Outline each blood parasite and name the species.
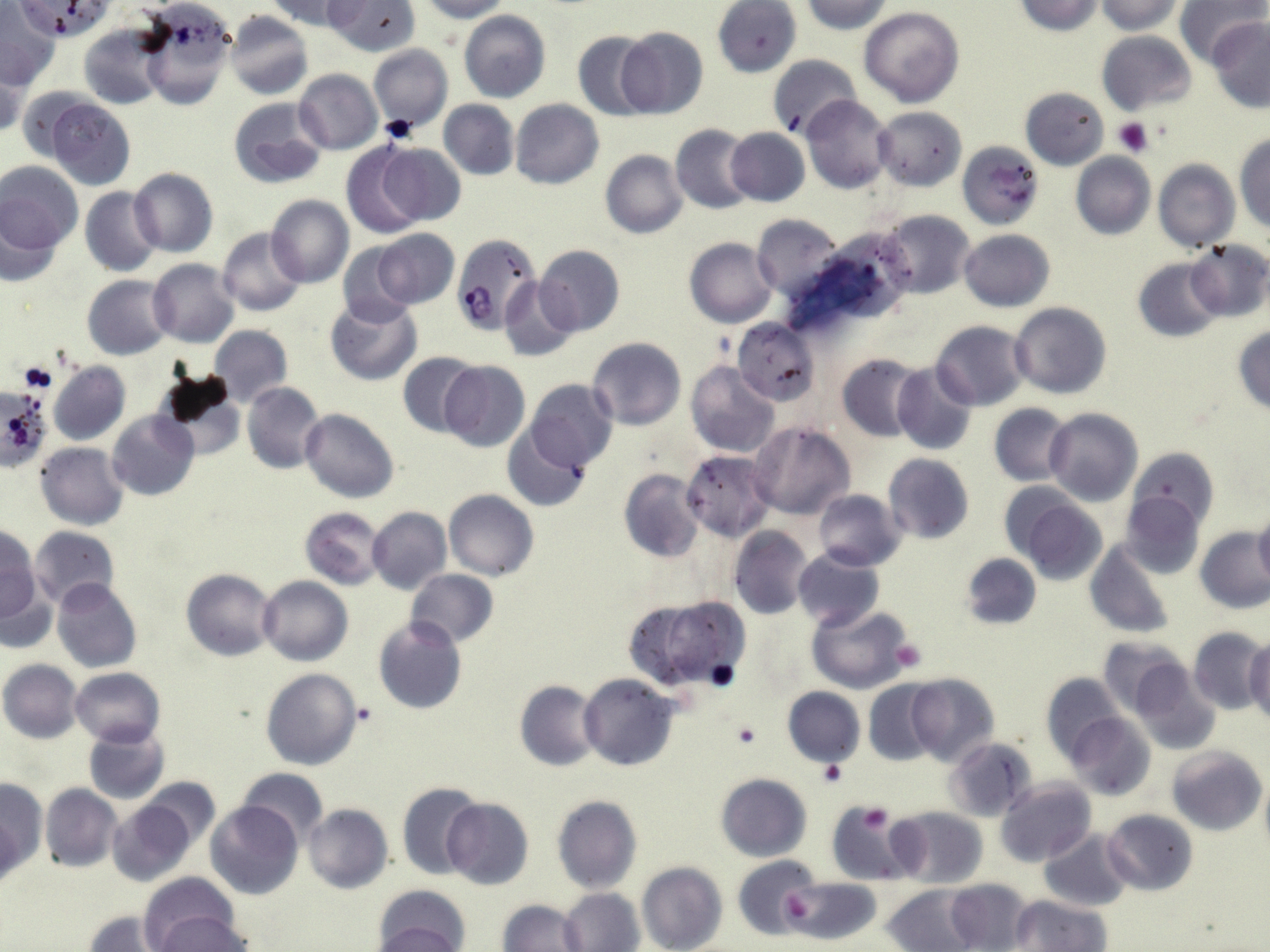

Approximate bounding boxes as named x1/y1/x2/y2 corners in pixels.
Plasmodium falciparum-infected red blood cells: (x1=451, y1=234, x2=542, y2=332).
No Plasmodium ovale, Plasmodium malariae, Plasmodium vivax, Babesia divergens, or Trypanosoma brucei observed.

slide_level_diagnosis: Plasmodium falciparum
uninfected_red_blood_cell_locations: 'approximate bounding boxes as named x1/y1/x2/y2 corners in pixels: (x1=15, y1=0, x2=111, y2=40), (x1=266, y1=0, x2=355, y2=30), (x1=324, y1=0, x2=420, y2=55), (x1=418, y1=0, x2=513, y2=21), (x1=712, y1=0, x2=800, y2=77), (x1=799, y1=0, x2=896, y2=34), (x1=1013, y1=0, x2=1103, y2=35), (x1=1097, y1=0, x2=1185, y2=34), (x1=1176, y1=0, x2=1264, y2=65), (x1=135, y1=4, x2=235, y2=111), (x1=0, y1=5, x2=58, y2=87), (x1=859, y1=6, x2=964, y2=106), (x1=224, y1=9, x2=313, y2=99), (x1=459, y1=10, x2=551, y2=103), (x1=451, y1=11, x2=536, y2=183), (x1=1208, y1=18, x2=1270, y2=113), (x1=80, y1=23, x2=168, y2=109), (x1=615, y1=26, x2=709, y2=119), (x1=573, y1=30, x2=657, y2=120), (x1=1096, y1=31, x2=1198, y2=117), (x1=369, y1=44, x2=452, y2=133), (x1=0, y1=49, x2=28, y2=138), (x1=767, y1=54, x2=862, y2=139), (x1=293, y1=69, x2=382, y2=155), (x1=14, y1=85, x2=95, y2=163), (x1=1019, y1=87, x2=1109, y2=168), (x1=801, y1=95, x2=894, y2=195), (x1=46, y1=97, x2=137, y2=190), (x1=227, y1=97, x2=327, y2=190), (x1=439, y1=99, x2=519, y2=179), (x1=510, y1=99, x2=603, y2=189), (x1=874, y1=106, x2=966, y2=190), (x1=671, y1=124, x2=758, y2=214), (x1=725, y1=128, x2=810, y2=206), (x1=1234, y1=131, x2=1270, y2=233), (x1=958, y1=137, x2=1045, y2=228), (x1=376, y1=142, x2=466, y2=226), (x1=341, y1=143, x2=430, y2=238), (x1=601, y1=150, x2=688, y2=239), (x1=1071, y1=152, x2=1154, y2=239), (x1=1153, y1=158, x2=1239, y2=252), (x1=1, y1=162, x2=83, y2=256), (x1=129, y1=167, x2=218, y2=257), (x1=80, y1=187, x2=162, y2=277), (x1=266, y1=196, x2=353, y2=288), (x1=0, y1=202, x2=68, y2=287), (x1=878, y1=210, x2=977, y2=300), (x1=753, y1=213, x2=844, y2=301), (x1=217, y1=228, x2=306, y2=317), (x1=371, y1=228, x2=460, y2=310), (x1=959, y1=229, x2=1055, y2=312), (x1=685, y1=237, x2=778, y2=327), (x1=1184, y1=241, x2=1270, y2=322), (x1=336, y1=242, x2=418, y2=326), (x1=535, y1=244, x2=626, y2=335), (x1=1132, y1=257, x2=1223, y2=342), (x1=148, y1=260, x2=239, y2=348), (x1=83, y1=274, x2=175, y2=358), (x1=500, y1=276, x2=579, y2=361), (x1=325, y1=294, x2=423, y2=386), (x1=1008, y1=301, x2=1112, y2=399), (x1=732, y1=318, x2=819, y2=405), (x1=930, y1=321, x2=1030, y2=411), (x1=1232, y1=325, x2=1270, y2=416), (x1=209, y1=326, x2=292, y2=407), (x1=588, y1=337, x2=686, y2=431), (x1=398, y1=352, x2=482, y2=438), (x1=837, y1=353, x2=927, y2=441), (x1=48, y1=361, x2=130, y2=445), (x1=439, y1=361, x2=530, y2=453), (x1=685, y1=361, x2=780, y2=458), (x1=892, y1=363, x2=979, y2=455), (x1=153, y1=371, x2=246, y2=460), (x1=525, y1=378, x2=619, y2=471), (x1=242, y1=382, x2=325, y2=473), (x1=989, y1=403, x2=1073, y2=484), (x1=1044, y1=408, x2=1143, y2=505), (x1=301, y1=409, x2=399, y2=503), (x1=107, y1=411, x2=199, y2=501), (x1=748, y1=421, x2=856, y2=521), (x1=503, y1=424, x2=592, y2=513), (x1=36, y1=442, x2=129, y2=530), (x1=1127, y1=447, x2=1219, y2=534), (x1=680, y1=450, x2=773, y2=540), (x1=884, y1=453, x2=974, y2=544), (x1=618, y1=469, x2=705, y2=563), (x1=443, y1=489, x2=540, y2=580), (x1=814, y1=489, x2=904, y2=571), (x1=1120, y1=490, x2=1206, y2=579), (x1=1014, y1=494, x2=1108, y2=586), (x1=299, y1=507, x2=385, y2=588), (x1=366, y1=507, x2=452, y2=595), (x1=1253, y1=510, x2=1270, y2=587), (x1=0, y1=526, x2=42, y2=628), (x1=29, y1=526, x2=119, y2=611), (x1=730, y1=527, x2=815, y2=619), (x1=1195, y1=528, x2=1270, y2=614), (x1=1085, y1=539, x2=1177, y2=638), (x1=793, y1=548, x2=884, y2=628), (x1=959, y1=553, x2=1041, y2=631), (x1=181, y1=569, x2=278, y2=661), (x1=405, y1=569, x2=499, y2=647), (x1=0, y1=576, x2=56, y2=655), (x1=258, y1=576, x2=353, y2=666), (x1=53, y1=577, x2=142, y2=673), (x1=629, y1=593, x2=749, y2=688), (x1=806, y1=602, x2=916, y2=692), (x1=372, y1=615, x2=467, y2=714), (x1=1187, y1=627, x2=1266, y2=716), (x1=1098, y1=636, x2=1190, y2=717), (x1=1246, y1=638, x2=1270, y2=726), (x1=1, y1=660, x2=83, y2=743), (x1=1129, y1=663, x2=1222, y2=756), (x1=70, y1=667, x2=164, y2=747), (x1=262, y1=668, x2=363, y2=770), (x1=904, y1=672, x2=1000, y2=766), (x1=1041, y1=673, x2=1124, y2=763), (x1=579, y1=674, x2=679, y2=771), (x1=864, y1=679, x2=941, y2=765), (x1=515, y1=680, x2=603, y2=772), (x1=782, y1=687, x2=865, y2=768), (x1=1065, y1=712, x2=1156, y2=802), (x1=83, y1=726, x2=170, y2=803), (x1=946, y1=738, x2=1038, y2=821), (x1=1168, y1=746, x2=1266, y2=835), (x1=237, y1=769, x2=328, y2=846), (x1=1259, y1=771, x2=1270, y2=862), (x1=716, y1=774, x2=811, y2=861), (x1=140, y1=777, x2=219, y2=849), (x1=0, y1=778, x2=46, y2=878), (x1=995, y1=778, x2=1095, y2=868), (x1=398, y1=781, x2=486, y2=879), (x1=40, y1=784, x2=121, y2=872), (x1=552, y1=795, x2=642, y2=894), (x1=442, y1=798, x2=534, y2=889), (x1=829, y1=799, x2=910, y2=883), (x1=107, y1=800, x2=195, y2=886), (x1=206, y1=802, x2=304, y2=901), (x1=304, y1=803, x2=393, y2=894), (x1=890, y1=807, x2=987, y2=888), (x1=1103, y1=809, x2=1198, y2=894), (x1=1, y1=810, x2=26, y2=894), (x1=1041, y1=830, x2=1133, y2=910), (x1=734, y1=855, x2=820, y2=941), (x1=636, y1=863, x2=728, y2=952), (x1=136, y1=872, x2=242, y2=946), (x1=786, y1=878, x2=879, y2=946), (x1=945, y1=879, x2=1033, y2=951), (x1=884, y1=883, x2=980, y2=952), (x1=372, y1=886, x2=471, y2=952), (x1=560, y1=888, x2=644, y2=952), (x1=1011, y1=895, x2=1109, y2=951), (x1=498, y1=899, x2=586, y2=951), (x1=148, y1=909, x2=249, y2=951), (x1=82, y1=912, x2=173, y2=951), (x1=370, y1=922, x2=467, y2=952)'
stain: May-Grünwald-Giemsa
modality: optical microscopy
field_of_view: single
magnification: 1000x
preparation: thin blood film
image_size: 1270×952 pixels
platelet_locations: 'approximate bounding boxes as named x1/y1/x2/y2 corners in pixels: (x1=381, y1=114, x2=421, y2=144), (x1=1113, y1=117, x2=1154, y2=156), (x1=18, y1=362, x2=56, y2=393), (x1=889, y1=638, x2=927, y2=673), (x1=705, y1=660, x2=739, y2=691), (x1=730, y1=720, x2=762, y2=748), (x1=818, y1=758, x2=846, y2=787), (x1=857, y1=805, x2=895, y2=834), (x1=783, y1=894, x2=814, y2=924)'